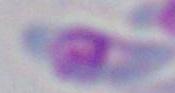

identification = Toxoplasma gondii
modality = photomicrograph
magnification = 1000x